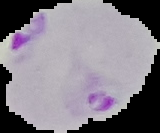
image size = 160×133 pixels
preparation = thin blood smear
image type = segmented cell region with the area outside set to black
result = Plasmodium parasites identified